Assess this cell for malaria.
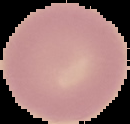

Uninfected.

Summary:
  - Image size: 130×124 pixels
  - Image type: segmented cell region with the area outside set to black
  - Preparation: thin blood film